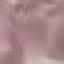

Summary:
  - Result: no malaria parasites detected
  - Capture: smartphone through the microscope eyepiece
  - Preparation: thin blood smear
  - Stain: Giemsa
  - Image type: cell patch, automatically extracted from a larger field of view and resized to 64 × 64 pixels